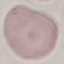

result = negative for malaria parasites
stain = Giemsa
capture = smartphone through the microscope eyepiece
preparation = thin blood film
image type = cell patch, automatically extracted from a larger field of view and resized to 64 × 64 pixels